Evaluate for malaria.
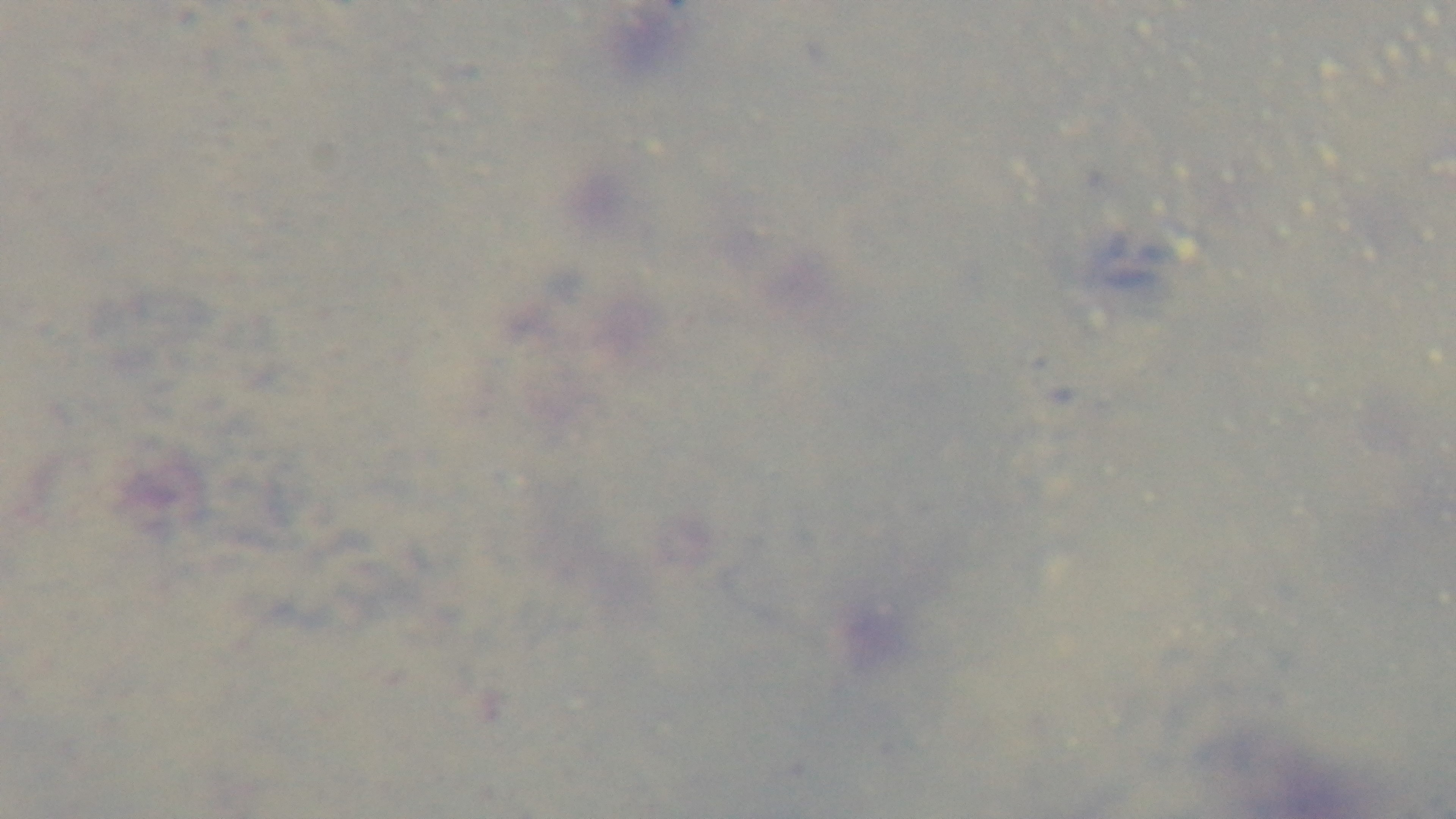
Negative.

Summary:
  - Modality: light microscopy
  - Preparation: thick
  - Stain: Giemsa
  - Objective: 100x oil immersion
  - Field of view: single
  - Capture: mounted 4K digital camera